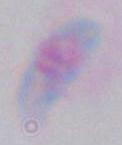
magnification: 1000x
identification: Toxoplasma gondii
modality: micrograph